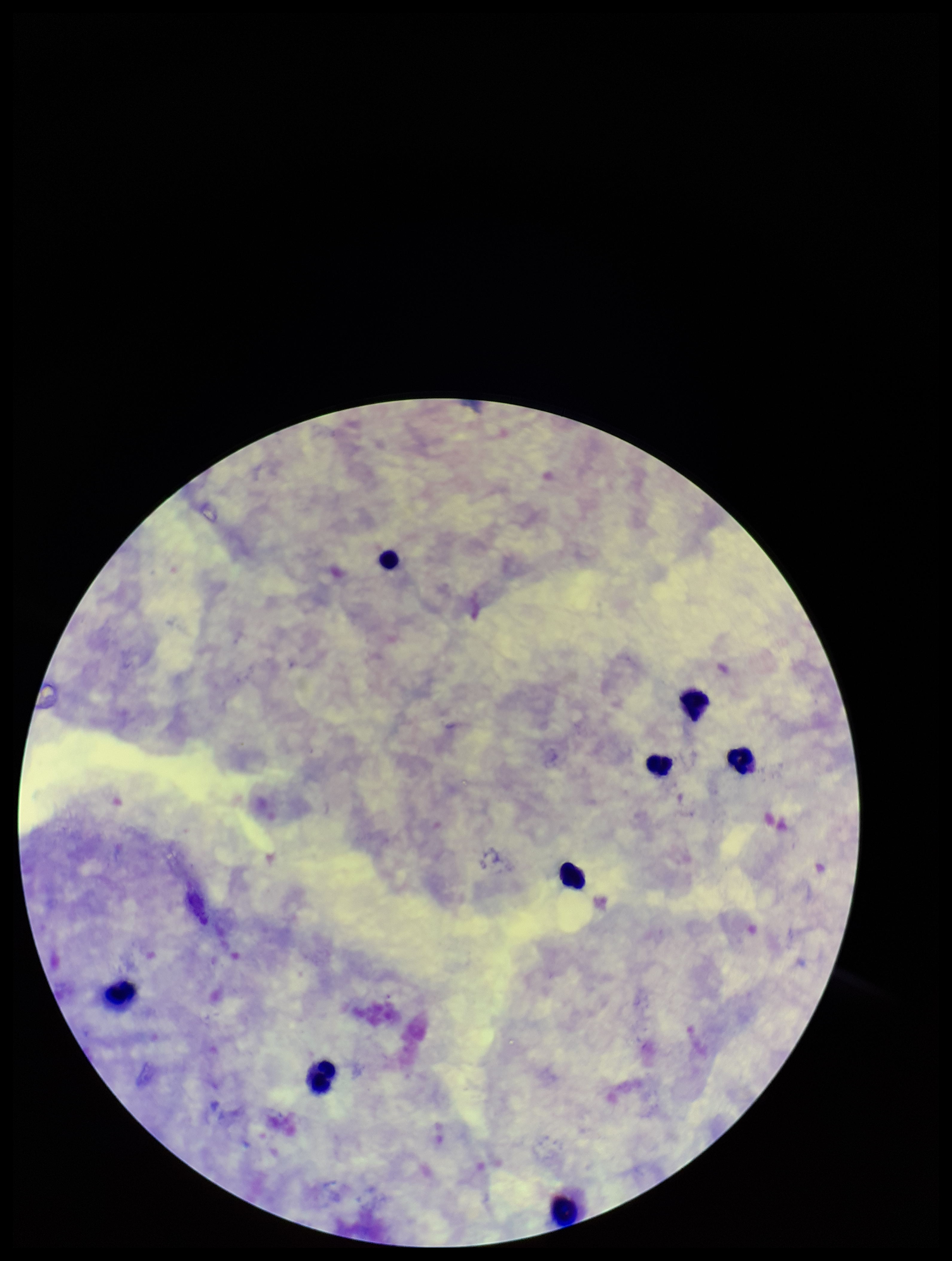 Leukocyte count: 8. Giemsa stain. Photographed through the microscope eyepiece with a smartphone camera. Parasite count: 0. Plasmodium parasites: none seen. Preparation: thick. Image is 952×1261 pixels. One field from this slide. Patient malaria status: negative.